Locate and identify every blood parasite.
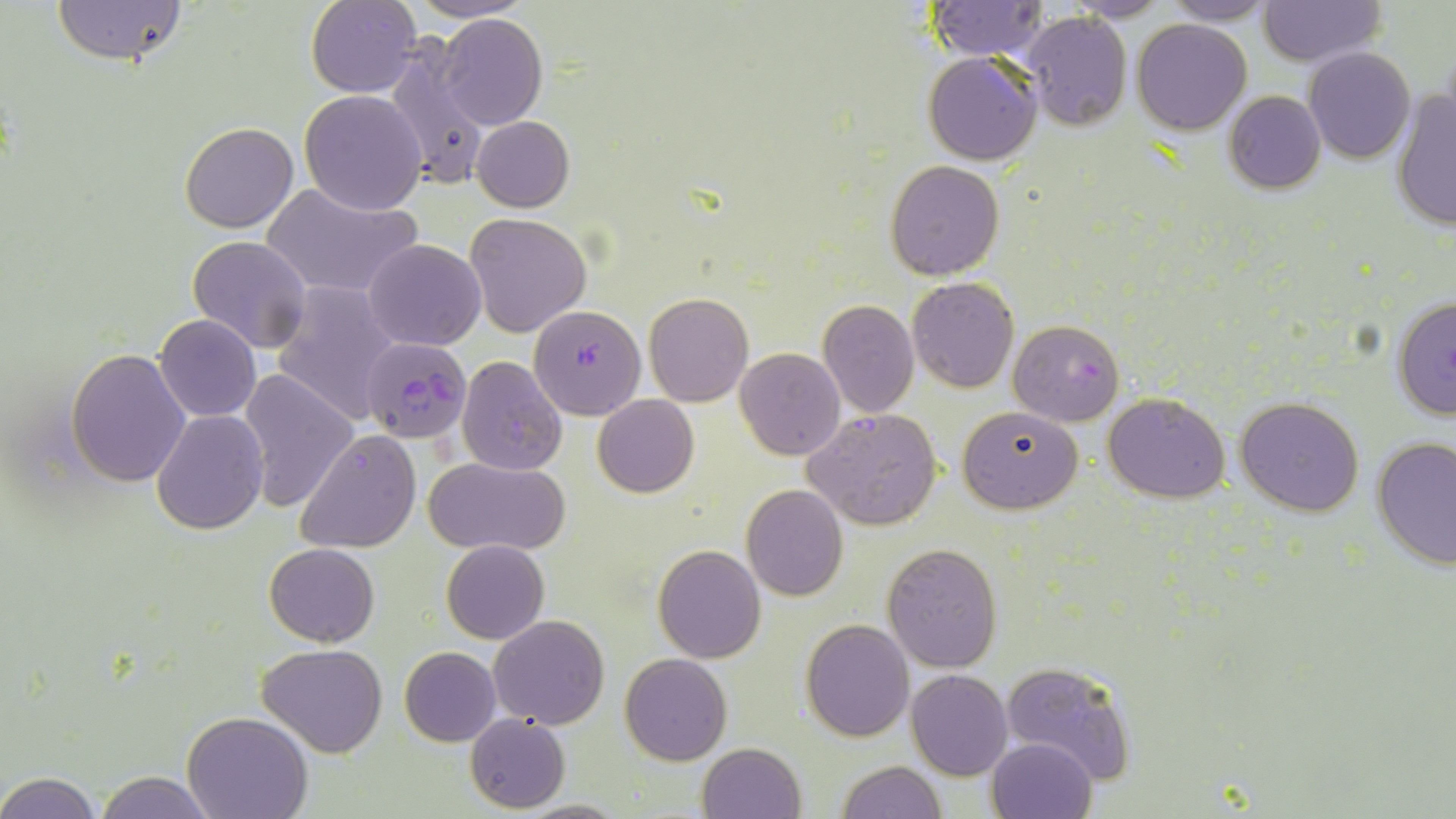

Approximate bounding boxes as named x1/y1/x2/y2 corners in pixels.
Plasmodium falciparum-infected red blood cells: (x1=529, y1=304, x2=646, y2=419), (x1=1008, y1=318, x2=1125, y2=426), (x1=360, y1=335, x2=470, y2=442).
No Plasmodium ovale, Plasmodium malariae, Plasmodium vivax, Babesia divergens, or Trypanosoma brucei observed.

{
  "slide_level_diagnosis": "Plasmodium falciparum",
  "uninfected_red_blood_cell_locations": "approximate bounding boxes as named x1/y1/x2/y2 corners in pixels: (x1=50, y1=0, x2=190, y2=69), (x1=306, y1=0, x2=422, y2=98), (x1=402, y1=0, x2=536, y2=24), (x1=1161, y1=0, x2=1279, y2=25), (x1=927, y1=1, x2=1049, y2=60), (x1=1065, y1=1, x2=1171, y2=22), (x1=1258, y1=1, x2=1385, y2=67), (x1=1022, y1=11, x2=1133, y2=131), (x1=435, y1=13, x2=550, y2=130), (x1=1133, y1=19, x2=1251, y2=135), (x1=385, y1=42, x2=488, y2=192), (x1=1303, y1=47, x2=1416, y2=164), (x1=924, y1=51, x2=1042, y2=165), (x1=299, y1=90, x2=428, y2=215), (x1=1391, y1=90, x2=1456, y2=232), (x1=1224, y1=91, x2=1325, y2=193), (x1=471, y1=116, x2=575, y2=212), (x1=180, y1=121, x2=299, y2=233), (x1=885, y1=161, x2=1003, y2=280), (x1=261, y1=183, x2=422, y2=300), (x1=465, y1=211, x2=592, y2=338), (x1=188, y1=236, x2=312, y2=354), (x1=365, y1=240, x2=486, y2=350), (x1=906, y1=278, x2=1018, y2=393), (x1=272, y1=281, x2=401, y2=425), (x1=645, y1=293, x2=752, y2=407), (x1=1390, y1=296, x2=1456, y2=421), (x1=818, y1=300, x2=919, y2=418), (x1=154, y1=314, x2=260, y2=423), (x1=67, y1=347, x2=191, y2=486), (x1=734, y1=348, x2=845, y2=460), (x1=458, y1=356, x2=567, y2=476), (x1=238, y1=366, x2=358, y2=512), (x1=1103, y1=391, x2=1230, y2=502), (x1=593, y1=394, x2=698, y2=496), (x1=1235, y1=396, x2=1365, y2=517), (x1=956, y1=405, x2=1083, y2=513), (x1=804, y1=408, x2=943, y2=530), (x1=150, y1=410, x2=268, y2=535), (x1=298, y1=428, x2=420, y2=553), (x1=1373, y1=439, x2=1456, y2=572), (x1=425, y1=457, x2=568, y2=556), (x1=742, y1=484, x2=849, y2=601), (x1=442, y1=539, x2=548, y2=643), (x1=265, y1=543, x2=379, y2=647), (x1=883, y1=543, x2=1001, y2=671), (x1=652, y1=545, x2=767, y2=664), (x1=488, y1=615, x2=610, y2=729), (x1=801, y1=619, x2=915, y2=742), (x1=257, y1=643, x2=387, y2=756), (x1=400, y1=647, x2=501, y2=747), (x1=620, y1=652, x2=733, y2=765), (x1=1002, y1=659, x2=1137, y2=784), (x1=906, y1=669, x2=1012, y2=779), (x1=182, y1=712, x2=313, y2=819), (x1=465, y1=714, x2=569, y2=812), (x1=987, y1=736, x2=1097, y2=819), (x1=697, y1=742, x2=805, y2=819), (x1=835, y1=760, x2=945, y2=818), (x1=2, y1=771, x2=103, y2=817), (x1=96, y1=772, x2=219, y2=818)",
  "stain": "May-Grünwald-Giemsa",
  "field_of_view": "one of a larger specimen",
  "image_size": "1456×819 pixels",
  "preparation": "thin blood film",
  "modality": "optical microscopy",
  "magnification": "1000x"
}